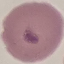 Result: no malaria parasites seen. Giemsa-stained preparation. Acquired by smartphone through the microscope eyepiece. Cell patch, automatically extracted from a larger field of view and resized to 64 × 64 pixels. Thin blood smear.